Outline each blood parasite and name the species.
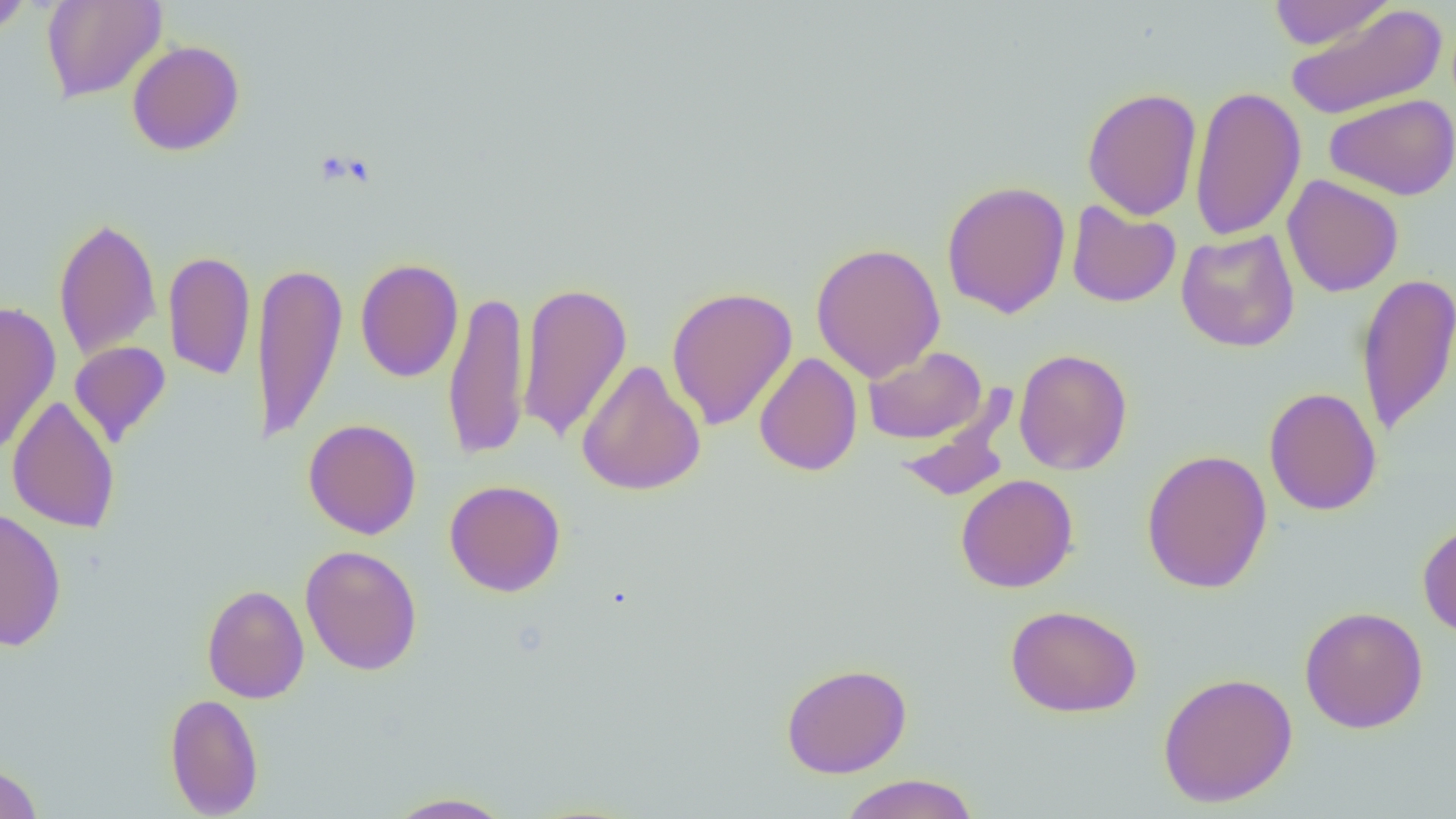

No blood parasites seen.

Approximate bounding boxes as [x1, y1, x2, y2] in pixels. Uninfected red blood cell locations: [0, 0, 35, 37], [41, 0, 167, 103], [1267, 0, 1394, 50], [1285, 4, 1447, 119], [127, 40, 244, 156], [1189, 84, 1307, 242], [1081, 86, 1202, 221], [1325, 93, 1456, 201], [1282, 175, 1404, 298], [941, 180, 1071, 319], [1066, 199, 1181, 308], [53, 215, 162, 362], [1176, 229, 1300, 352], [810, 242, 945, 382], [163, 250, 256, 381], [354, 257, 464, 383], [252, 258, 347, 447], [1355, 272, 1456, 437], [516, 280, 633, 444], [666, 286, 798, 431], [442, 289, 530, 461], [0, 300, 62, 456], [69, 341, 171, 447], [862, 346, 987, 444], [1013, 348, 1133, 476], [753, 352, 863, 477], [576, 358, 706, 496], [1263, 386, 1382, 516], [895, 390, 1019, 503], [7, 395, 120, 534], [303, 418, 421, 539], [1140, 448, 1272, 595], [955, 474, 1078, 593], [444, 479, 566, 597], [0, 506, 67, 652], [1417, 521, 1456, 637], [300, 544, 422, 676], [201, 584, 310, 704], [1005, 604, 1143, 718], [1300, 605, 1428, 734], [781, 662, 912, 778], [1157, 671, 1298, 807], [165, 692, 264, 818], [0, 762, 43, 819], [838, 773, 980, 819], [383, 792, 517, 818]. Slide-level diagnosis: negative for blood parasites. Single field of view. Thin blood film. 1000x magnification. Optical microscopy. Image is 1456×819 pixels.